Report the malaria status of this cell.
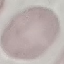

It is uninfected.

Thin blood smear. Giemsa stain. Cell patch, automatically extracted from a larger field of view and resized to 64 × 64 pixels. Acquired by smartphone through the microscope eyepiece.